Assess the morphology of the red blood cells.
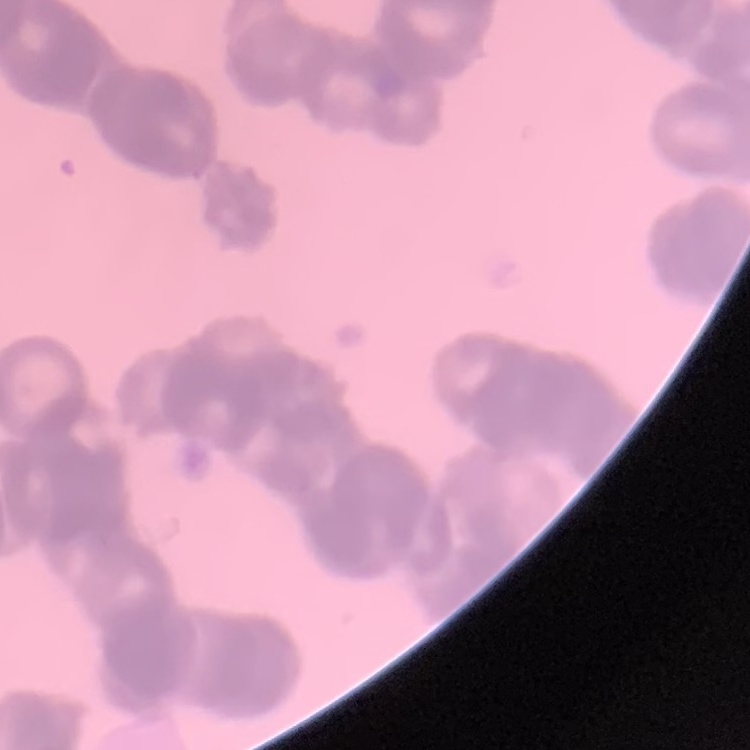
Rouleaux formation.

Summary:
  - Stain: Field's or Giemsa
  - Image type: square crop of a larger photomicrograph
  - Preparation: thin blood film